Describe the morphology of the erythrocytes.
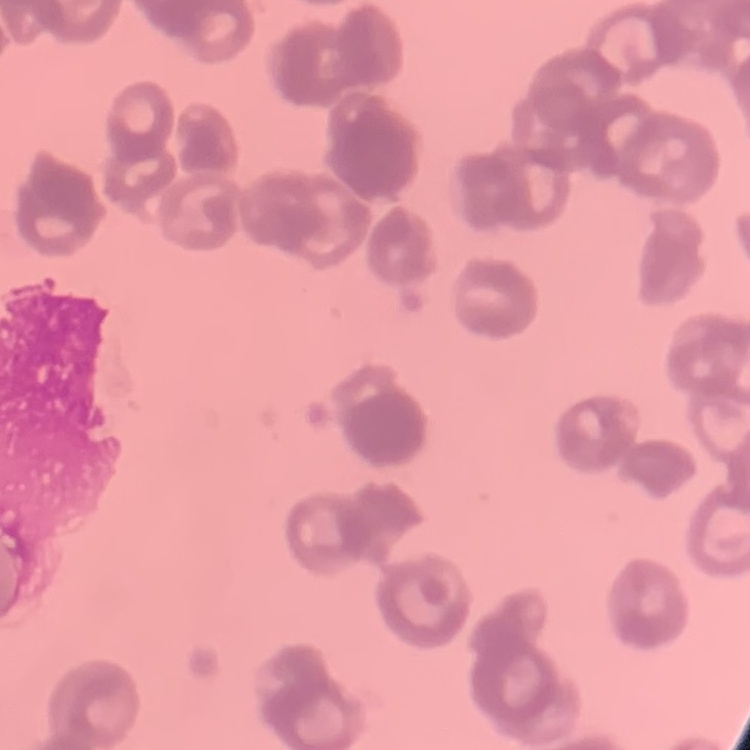
They show rouleaux formation.

Summary:
  - Image type: square crop of a larger photomicrograph
  - Preparation: thin blood smear
  - Stain: Field's or Giemsa